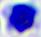

Summary:
  - Modality: micrograph
  - Identification: white blood cell
  - Magnification: 400x